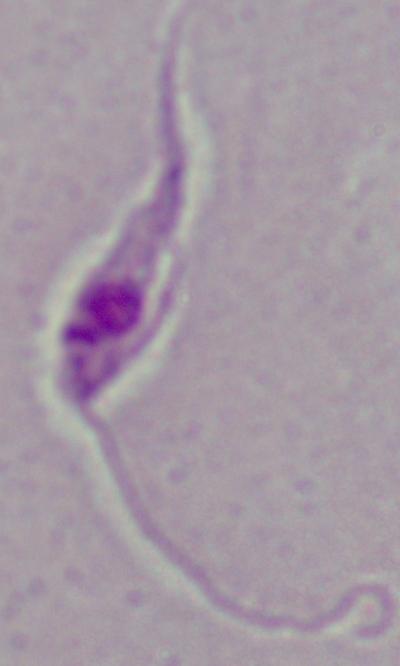

Summary:
  - Identification: Leishmania
  - Modality: photomicrograph
  - Magnification: 1000x